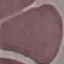
{
  "malaria_status": "uninfected",
  "capture": "smartphone through the microscope eyepiece",
  "preparation": "thin blood smear",
  "stain": "Giemsa",
  "image_type": "cell patch, automatically extracted from a larger field of view and resized to 64 × 64 pixels"
}